Classify the preparation.
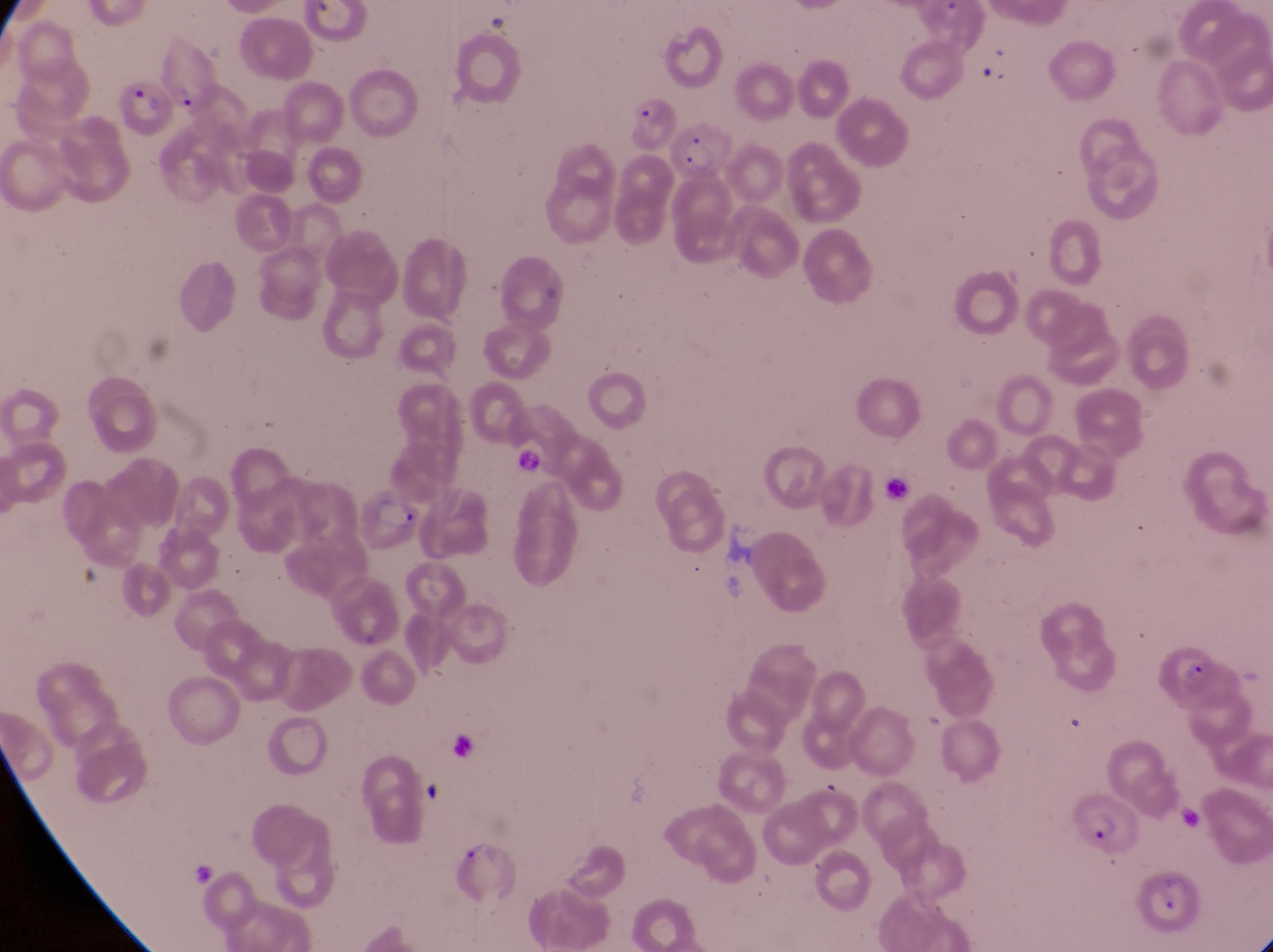

Thin blood smear.

{
  "image_size": "1273×952 pixels",
  "capture": "smartphone photograph through the eyepiece of an Olympus CX-23 microscope",
  "field_of_view": "single",
  "country": "Uganda",
  "artifact_platelet_like_body_stain_precipitate_or_debris_locations": "approximate bounding boxes as left top right bottom in pixels: 519 442 549 482; 881 469 913 504; 419 774 454 811; 183 859 220 887",
  "parasitised_red_blood_cell_locations": "approximate bounding boxes as left top right bottom in pixels: 156 46 216 106; 110 75 173 143; 619 92 674 147; 674 122 736 184; 357 480 424 552; 1148 642 1222 707; 1081 789 1139 852; 449 834 523 908; 1139 869 1213 934",
  "magnification": "1000x"
}